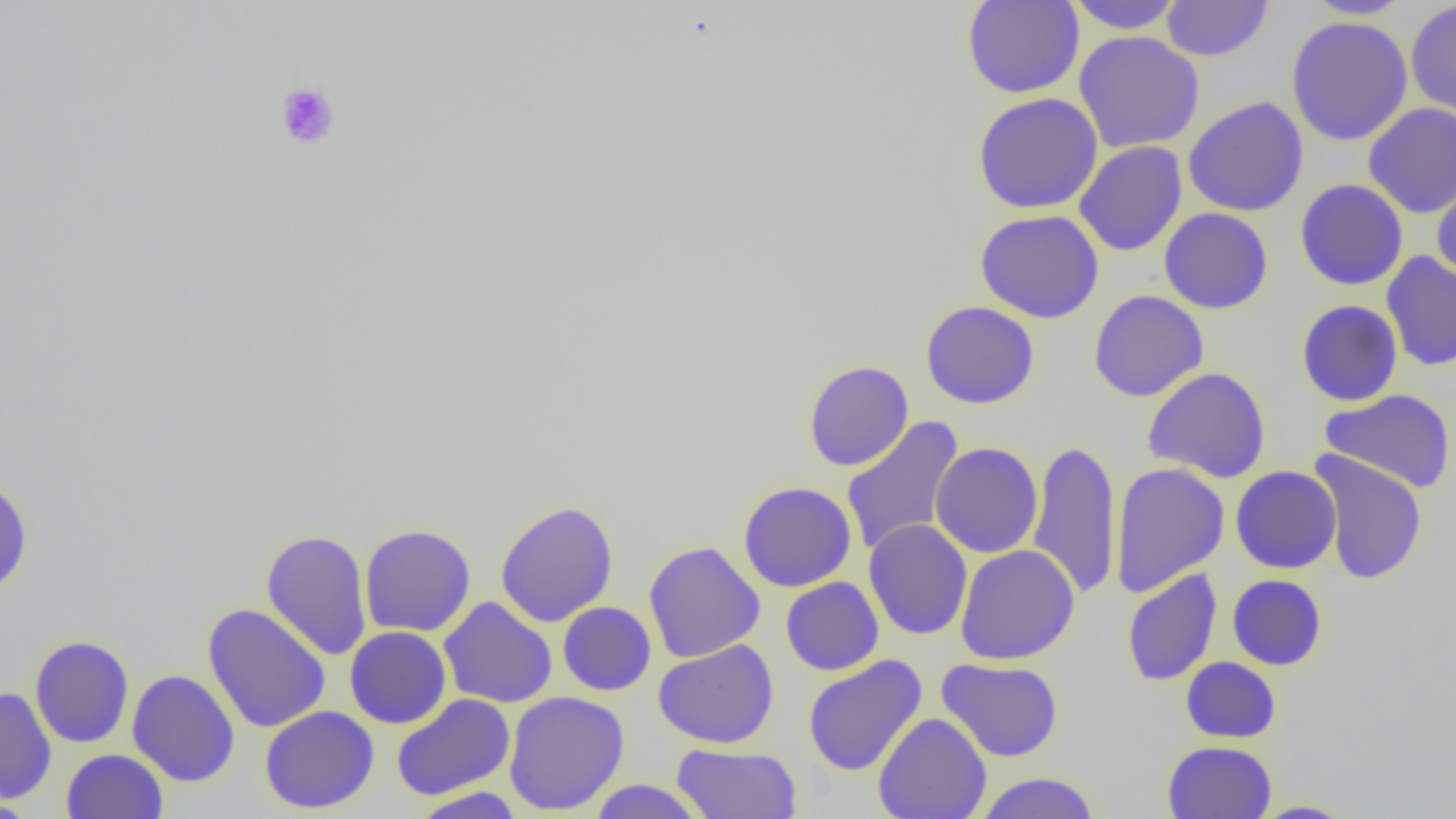
slide_level_diagnosis: negative for blood parasites
field_of_view: single
uninfected_red_blood_cell_locations: 'approximate bounding boxes as (x1, y1, x2, y2) in pixels: (961, 0, 1084, 98), (1066, 0, 1186, 34), (1161, 0, 1273, 62), (1302, 0, 1414, 20), (1405, 1, 1456, 117), (1286, 15, 1413, 146), (1073, 31, 1205, 153), (972, 92, 1103, 215), (1183, 96, 1308, 217), (1362, 103, 1456, 218), (1074, 141, 1187, 256), (1431, 171, 1456, 284), (1295, 179, 1408, 290), (1159, 208, 1273, 314), (975, 209, 1104, 323), (1381, 251, 1456, 371), (1088, 290, 1209, 402), (1296, 300, 1403, 406), (921, 301, 1039, 409), (803, 360, 914, 472), (1142, 367, 1272, 484), (1320, 388, 1456, 494), (841, 416, 965, 557), (1027, 438, 1122, 601), (930, 442, 1043, 558), (1310, 450, 1428, 586), (1110, 462, 1230, 597), (1230, 466, 1341, 574), (0, 478, 33, 598), (738, 481, 856, 592), (495, 500, 619, 627), (863, 519, 973, 640), (359, 524, 476, 637), (261, 529, 373, 661), (643, 541, 765, 663), (955, 544, 1080, 665), (1122, 568, 1222, 686), (1227, 574, 1327, 670), (780, 577, 884, 676), (439, 597, 557, 708), (557, 602, 656, 696), (202, 603, 331, 733), (345, 626, 452, 728), (29, 635, 134, 747), (653, 639, 779, 748), (803, 655, 926, 776), (1181, 656, 1281, 743), (936, 658, 1064, 762), (127, 669, 240, 787), (0, 686, 57, 804), (503, 691, 630, 815), (391, 693, 515, 801), (260, 706, 379, 813), (873, 712, 992, 819), (1162, 741, 1277, 818), (671, 743, 802, 819), (61, 749, 168, 819), (973, 771, 1102, 818), (587, 779, 707, 819), (410, 787, 526, 818), (1249, 800, 1359, 818)'
preparation: thin blood film
modality: optical microscopy
magnification: 1000x
image_size: 1456×819 pixels
platelet_locations: 'approximate bounding boxes as (x1, y1, x2, y2) in pixels: (273, 80, 340, 150)'